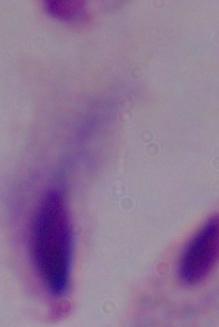

Summary:
  - Modality: photomicrograph
  - Identification: trichomonad
  - Magnification: 1000x